Identify the preparation type.
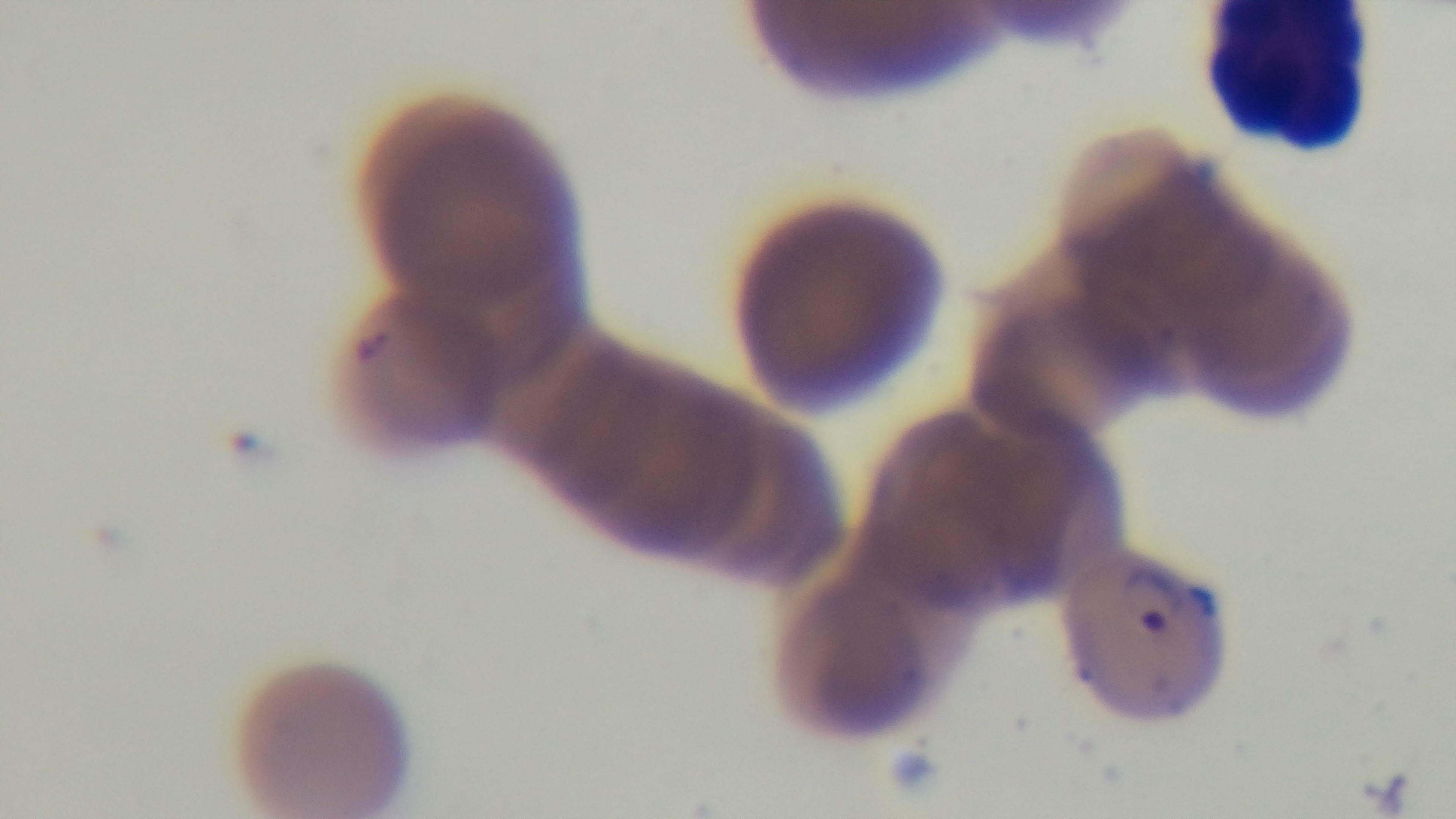
A thin smear.

objective: 100x oil immersion
field_of_view: one from the slide
malaria_status: positive
capture: mounted 4K digital camera
stain: Giemsa
modality: light microscopy